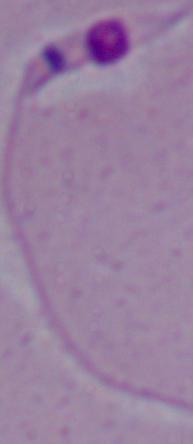 Captured at 1000x magnification. Micrograph. A Leishmania parasite is shown.